Locate every malaria parasite.
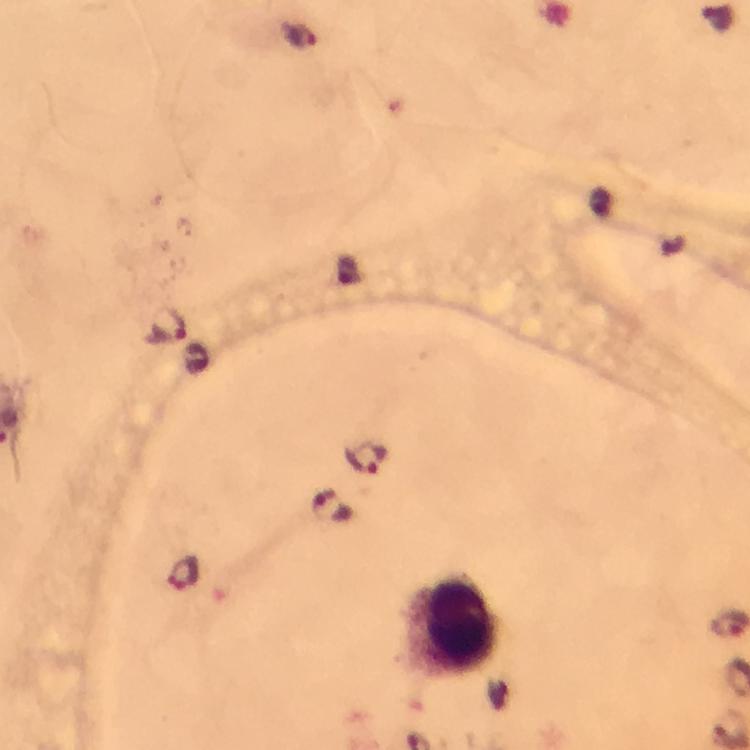
Approximate centers as {x, y} in pixels.
Malaria parasites: {303, 37}, {169, 323}, {366, 457}, {331, 508}, {184, 574}.

Leukocyte locations: {458, 626}. At 100x magnification. From a diagnostic examination for malaria. Photographed through the microscope with a smartphone camera. Immersion oil applied. Giemsa stain. Image is 750×750 pixels. A crop from one field of view. Thick smear.